Outline each Plasmodium ovale-infected red blood cell.
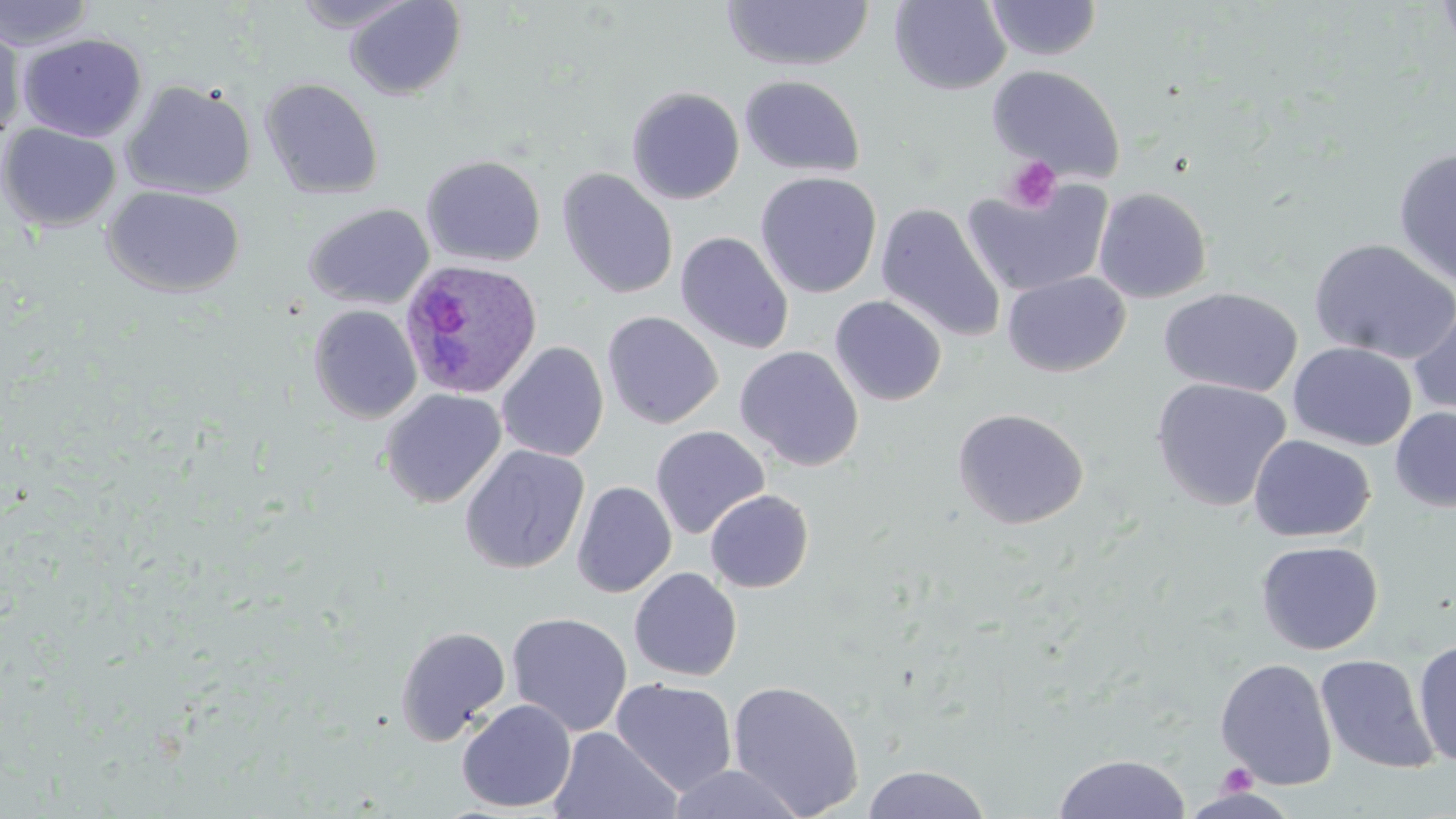

Approximate bounding boxes as (x1, y1, x2, y2) in pixels.
Plasmodium ovale-infected red blood cells: (399, 259, 542, 400).

Summary:
  - Platelet locations: (1003, 156, 1062, 213), (1219, 763, 1257, 797)
  - Uninfected red blood cell locations: (0, 0, 96, 50), (291, 0, 420, 33), (343, 0, 467, 101), (890, 0, 1011, 95), (987, 0, 1102, 61), (1436, 0, 1456, 59), (721, 1, 875, 71), (0, 19, 26, 145), (17, 33, 147, 143), (987, 64, 1126, 183), (740, 74, 866, 177), (259, 77, 384, 199), (120, 79, 256, 200), (626, 86, 745, 205), (0, 123, 122, 233), (1393, 146, 1456, 288), (420, 155, 546, 268), (557, 168, 678, 300), (755, 171, 882, 299), (963, 178, 1115, 297), (102, 185, 245, 297), (1094, 187, 1212, 303), (304, 203, 435, 310), (875, 203, 1006, 343), (675, 232, 794, 355), (1310, 239, 1456, 365), (1002, 271, 1131, 377), (1159, 286, 1303, 397), (830, 295, 947, 406), (1408, 299, 1456, 419), (307, 304, 422, 424), (601, 310, 723, 429), (496, 341, 608, 462), (1288, 342, 1417, 451), (735, 345, 864, 471), (1150, 377, 1292, 512), (380, 388, 506, 509), (951, 407, 1089, 529), (1390, 407, 1456, 513), (650, 425, 770, 539), (1248, 434, 1375, 542), (459, 444, 590, 575), (572, 481, 676, 598), (704, 489, 814, 593), (1256, 540, 1383, 655), (629, 567, 743, 681), (506, 612, 632, 737), (395, 625, 511, 744), (1412, 639, 1456, 768), (1315, 654, 1439, 774), (1215, 658, 1338, 790), (610, 678, 738, 795), (727, 679, 865, 818), (457, 699, 577, 813), (548, 727, 681, 819), (1053, 753, 1191, 818), (666, 764, 808, 819), (862, 764, 992, 819)
  - Slide-level diagnosis: Plasmodium ovale
  - Image size: 1456×819 pixels
  - Modality: light microscopy
  - Magnification: 1000x
  - Preparation: thin blood film
  - Stain: May-Grünwald-Giemsa
  - Field of view: single